Give the extent of all Plasmodium vivax-infected red blood cells.
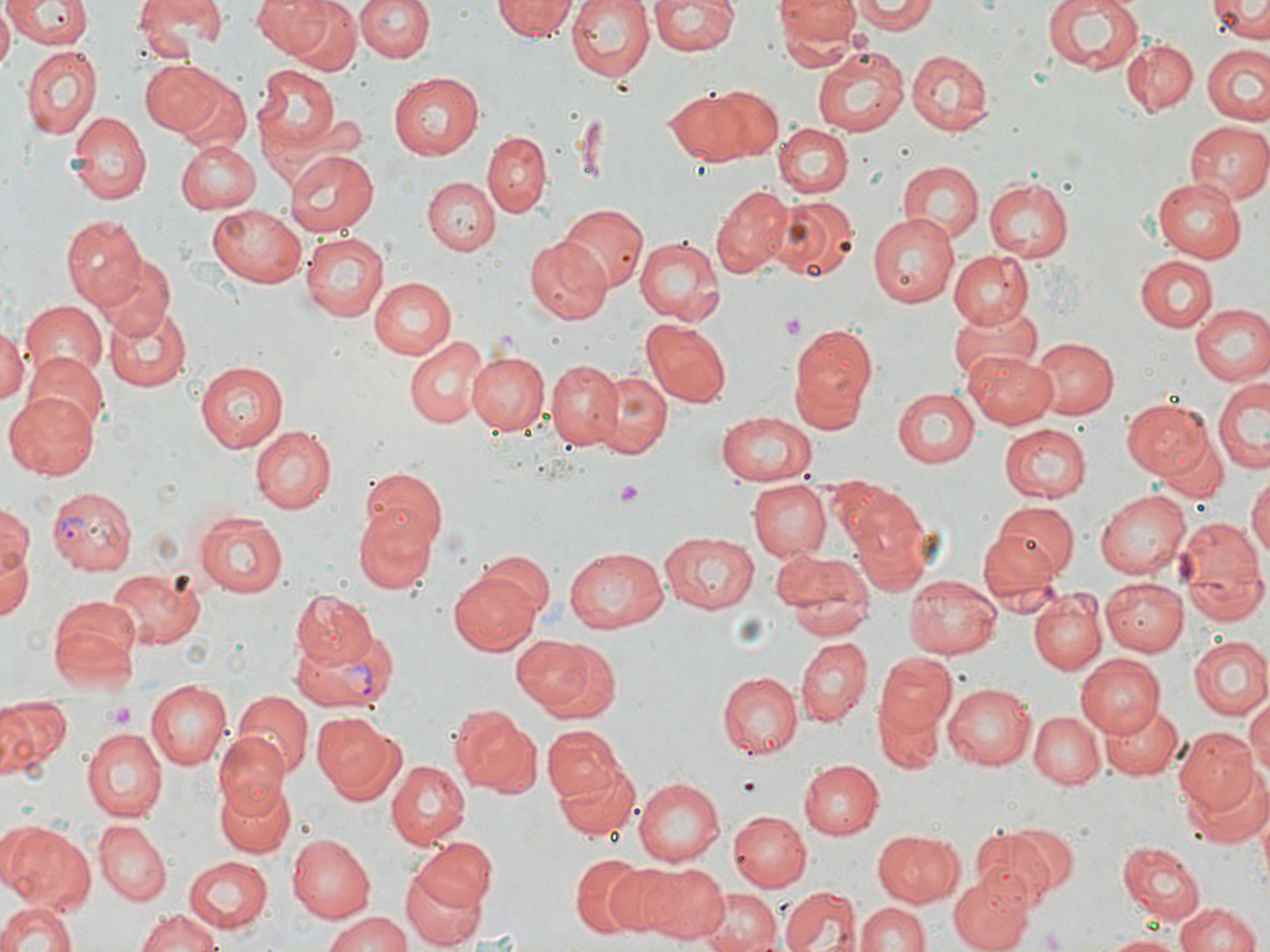
Approximate bounding boxes as (x1,y1)-(x2,y2) corner pairs in pixels.
Plasmodium vivax-infected red blood cells: (47,484)-(135,573), (291,627)-(396,716).

Summary:
  - Platelet locations: (780,313)-(806,340), (614,482)-(646,507), (107,704)-(139,728), (738,779)-(758,796), (1040,927)-(1066,950)
  - Uninfected red blood cell locations: (6,0)-(91,50), (138,0)-(227,48), (252,0)-(331,57), (355,0)-(433,63), (564,0)-(655,82), (650,0)-(738,58), (776,0)-(858,51), (855,0)-(935,34), (1041,0)-(1144,74), (1206,0)-(1270,40), (283,1)-(363,76), (492,1)-(575,42), (0,8)-(13,71), (1121,40)-(1197,116), (20,44)-(102,142), (1202,45)-(1270,125), (811,46)-(907,138), (907,50)-(993,136), (140,60)-(224,134), (256,62)-(338,156), (389,73)-(484,160), (175,80)-(250,155), (701,85)-(783,160), (663,87)-(752,166), (67,113)-(149,205), (1184,122)-(1269,206), (774,125)-(854,200), (483,131)-(551,214), (174,140)-(259,213), (284,147)-(378,236), (899,161)-(984,242), (424,176)-(499,254), (983,177)-(1075,262), (1151,178)-(1247,262), (712,184)-(792,275), (772,195)-(861,282), (559,204)-(646,293), (207,205)-(307,290), (868,212)-(959,309), (61,216)-(145,308), (299,233)-(387,321), (633,237)-(724,326), (523,238)-(610,324), (948,252)-(1034,329), (1137,254)-(1219,331), (93,257)-(176,338), (367,274)-(456,361), (18,302)-(108,382), (1189,303)-(1269,386), (105,304)-(192,392), (948,305)-(1039,384), (643,319)-(732,406), (0,323)-(25,404), (789,325)-(878,424), (1025,335)-(1118,419), (403,337)-(490,428), (466,350)-(551,435), (965,350)-(1059,426), (24,352)-(109,435), (546,360)-(624,451), (195,361)-(289,453), (587,369)-(671,458), (1212,376)-(1268,473), (7,389)-(100,477), (893,389)-(980,467), (1122,399)-(1217,480), (715,411)-(816,489), (250,424)-(336,513), (999,424)-(1091,504), (1154,426)-(1229,504), (359,465)-(449,554), (1248,474)-(1270,568), (747,478)-(831,561), (1095,489)-(1194,579), (850,501)-(931,596), (991,501)-(1078,582), (0,502)-(32,580), (356,508)-(438,594), (196,510)-(289,598), (1173,515)-(1269,622), (977,525)-(1065,601), (658,530)-(759,614), (1,537)-(35,627), (563,547)-(670,633), (770,548)-(874,640), (478,550)-(555,622), (104,567)-(206,649), (451,568)-(544,654), (903,576)-(1003,658), (1102,577)-(1188,655), (292,591)-(379,670), (1028,591)-(1107,675), (49,597)-(140,692), (512,634)-(612,719), (1187,636)-(1270,720), (793,637)-(870,725), (873,650)-(955,742), (1074,654)-(1163,738), (717,672)-(802,757), (145,680)-(231,769), (943,682)-(1035,769), (234,690)-(311,775), (0,697)-(67,779), (1246,698)-(1270,787), (875,699)-(944,776), (1100,699)-(1184,779), (453,710)-(542,798), (1029,712)-(1104,788), (314,714)-(406,804), (543,724)-(625,808), (82,727)-(167,821), (1173,727)-(1256,816), (212,731)-(289,813), (554,758)-(640,840), (387,759)-(472,847), (798,759)-(882,838), (1183,767)-(1266,848), (215,776)-(299,855), (634,777)-(725,866), (727,810)-(811,892), (95,821)-(171,903), (1,822)-(95,912), (972,824)-(1069,907), (287,831)-(379,923), (871,831)-(965,906), (410,839)-(496,917), (1119,843)-(1204,923), (570,854)-(648,937), (183,857)-(272,934), (601,861)-(688,935), (629,861)-(729,943), (399,865)-(489,950), (951,875)-(1031,952), (779,886)-(860,952), (698,891)-(779,952), (1,899)-(80,952), (857,900)-(931,952), (1175,901)-(1264,952), (134,910)-(225,952), (324,910)-(413,952), (1101,932)-(1185,952)
  - Slide-level diagnosis: Plasmodium vivax
  - Magnification: 1000x
  - Stain: May-Grünwald-Giemsa
  - Field of view: one of a larger specimen
  - Modality: light microscopy
  - Image size: 1270×952 pixels
  - Preparation: thin blood film